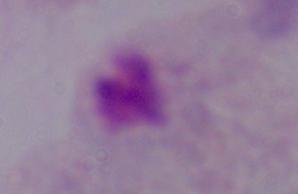

identification: trichomonad
magnification: 1000x
modality: photomicrograph